Identify the cell.
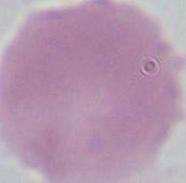

An erythrocyte.

{
  "magnification": "1000x",
  "modality": "micrograph"
}